Report the malaria status of this cell.
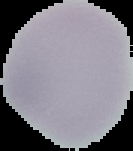

Uninfected.

Image is 133×151 pixels. From a thin blood smear. Cell region segmented out of the field of view; the surrounding area is masked to black.